Locate every Plasmodium parasite.
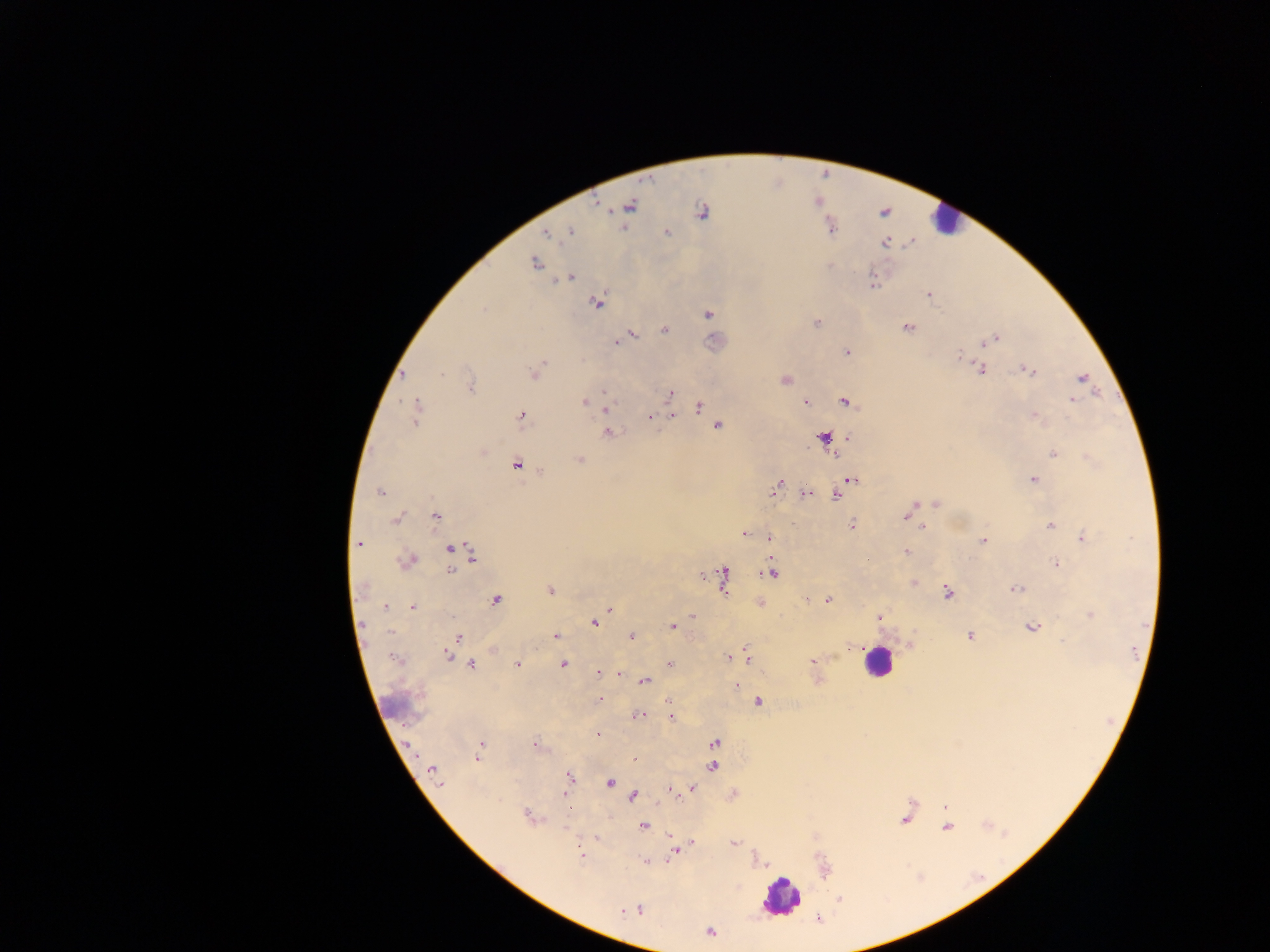

Approximate centers as {x, y} in pixels.
Plasmodium parasites: {630, 206}, {702, 211}, {570, 232}, {666, 232}, {546, 233}, {885, 242}, {535, 263}, {569, 278}, {873, 284}, {929, 294}, {597, 302}, {483, 309}, {708, 314}, {816, 323}, {907, 328}, {665, 330}, {630, 335}, {996, 338}, {990, 341}, {617, 342}, {983, 343}, {847, 352}, {960, 353}, {543, 362}, {981, 370}, {1029, 371}, {535, 373}, {1082, 377}, {784, 380}, {470, 387}, {605, 391}, {670, 393}, {1072, 399}, {584, 402}, {846, 402}, {806, 403}, {605, 407}, {699, 407}, {415, 411}, {521, 415}, {672, 416}, {1035, 416}, {650, 417}, {718, 426}, {608, 433}, {824, 437}, {483, 452}, {1053, 453}, {835, 455}, {579, 460}, {516, 466}, {852, 480}, {1034, 480}, {777, 486}, {379, 492}, {806, 493}, {836, 495}, {936, 504}, {911, 508}, {435, 516}, {907, 516}, {396, 519}, {851, 525}, {1051, 526}, {924, 527}, {744, 534}, {769, 538}, {1084, 538}, {983, 541}, {359, 544}, {449, 549}, {907, 551}, {472, 555}, {407, 561}, {1056, 564}, {451, 571}, {771, 572}, {724, 577}, {915, 582}, {1016, 589}, {550, 590}, {948, 593}, {496, 600}, {828, 600}, {760, 603}, {385, 607}, {412, 607}, {609, 609}, {1091, 615}, {692, 616}, {879, 618}, {594, 622}, {672, 627}, {1031, 627}, {391, 632}, {556, 636}, {631, 636}, {969, 636}, {458, 637}, {447, 655}, {747, 656}, {728, 658}, {395, 659}, {813, 660}, {669, 664}, {472, 665}, {517, 665}, {562, 665}, {598, 673}, {619, 674}, {644, 681}, {736, 685}, {600, 699}, {669, 702}, {758, 702}, {637, 715}, {671, 716}, {597, 735}, {714, 743}, {534, 745}, {481, 746}, {478, 758}, {634, 759}, {713, 767}, {432, 770}, {569, 777}, {609, 782}, {690, 789}, {674, 792}, {566, 794}, {633, 797}, {945, 806}, {528, 815}, {904, 820}, {643, 826}, {947, 827}, {735, 843}, {692, 844}, {674, 852}, {581, 856}, {840, 898}, {638, 910}, {622, 911}, {710, 932}.

{
  "field_of_view": "single",
  "capture": "mobile-phone photograph through a microscope",
  "leukocyte_locations": "approximate centers as {x, y} in pixels: {944, 220}, {877, 661}, {782, 898}",
  "image_size": "1270×952 pixels",
  "country": "Ghana",
  "preparation": "thick blood smear"
}